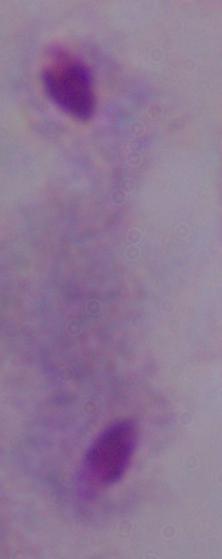

Summary:
  - Identification: trichomonad
  - Modality: photomicrograph
  - Magnification: 1000x